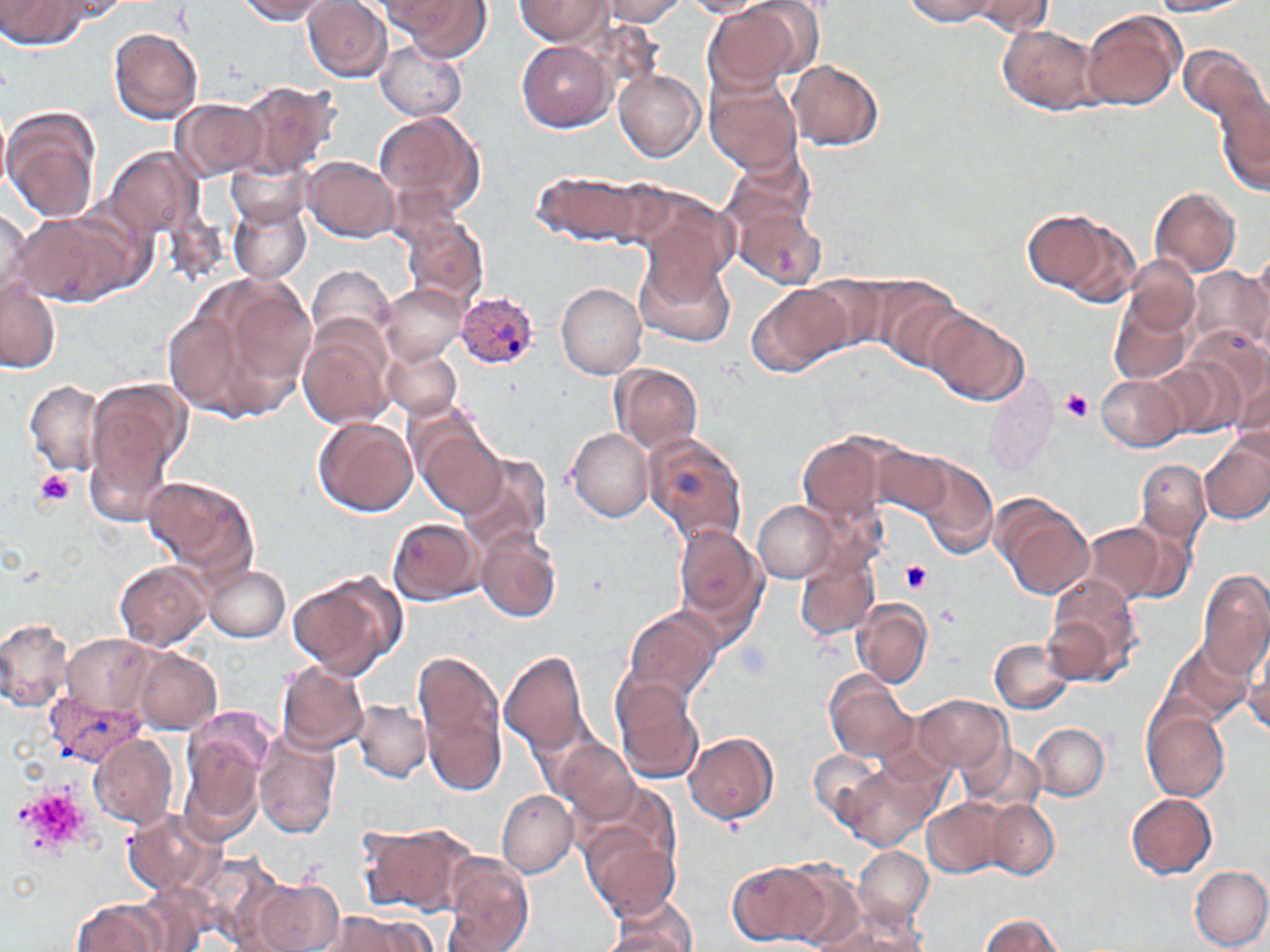

Approximate bounding boxes as [x1, y1, x2, y2] in pixels. Uninfected red blood cell locations: [2, 0, 91, 49], [235, 0, 340, 21], [515, 0, 612, 45], [1146, 0, 1253, 16], [304, 1, 395, 82], [390, 1, 493, 63], [597, 1, 688, 27], [681, 1, 768, 17], [904, 1, 1002, 25], [967, 1, 1049, 36], [704, 3, 815, 91], [1082, 11, 1185, 111], [998, 25, 1100, 115], [110, 27, 203, 123], [374, 39, 468, 123], [517, 41, 614, 131], [1180, 46, 1268, 163], [787, 59, 883, 150], [614, 69, 705, 162], [705, 74, 802, 175], [234, 80, 337, 178], [1214, 82, 1269, 201], [172, 98, 267, 181], [3, 106, 103, 225], [0, 110, 11, 193], [374, 110, 489, 225], [101, 145, 205, 246], [302, 156, 400, 242], [227, 160, 311, 229], [533, 168, 650, 246], [1152, 187, 1242, 275], [634, 188, 738, 296], [730, 200, 828, 291], [229, 203, 312, 283], [0, 207, 31, 307], [12, 209, 136, 308], [1021, 209, 1124, 296], [402, 215, 488, 306], [636, 249, 736, 349], [1245, 249, 1270, 340], [1125, 257, 1200, 336], [308, 266, 395, 349], [1189, 266, 1268, 354], [170, 274, 315, 424], [862, 275, 968, 369], [804, 278, 891, 358], [556, 281, 647, 379], [746, 281, 854, 378], [0, 282, 59, 374], [376, 283, 469, 365], [1110, 294, 1191, 385], [925, 308, 1030, 405], [298, 315, 395, 427], [1183, 327, 1268, 428], [382, 345, 464, 420], [1150, 358, 1245, 439], [612, 363, 703, 453], [1232, 372, 1270, 460], [1096, 375, 1183, 451], [82, 376, 187, 525], [23, 379, 107, 476], [984, 385, 1057, 478], [314, 416, 417, 517], [418, 422, 511, 517], [566, 426, 653, 522], [642, 432, 750, 549], [796, 433, 895, 526], [1200, 438, 1270, 524], [874, 444, 953, 518], [454, 449, 552, 557], [907, 454, 998, 558], [1135, 458, 1211, 549], [143, 475, 258, 578], [992, 494, 1095, 600], [754, 502, 838, 583], [764, 508, 872, 622], [389, 517, 484, 604], [1080, 520, 1171, 605], [673, 524, 768, 640], [476, 528, 562, 622], [796, 547, 882, 642], [114, 559, 210, 650], [202, 563, 291, 641], [1196, 569, 1270, 680], [287, 571, 403, 678], [1043, 576, 1144, 688], [853, 598, 932, 689], [620, 605, 723, 709], [0, 617, 76, 713], [1166, 633, 1259, 726], [63, 634, 153, 715], [1244, 634, 1270, 737], [990, 637, 1074, 713], [413, 648, 508, 794], [133, 649, 222, 733], [500, 651, 591, 757], [277, 662, 369, 754], [823, 671, 916, 761], [615, 676, 703, 783], [912, 695, 1010, 774], [354, 699, 430, 781], [1141, 705, 1230, 800], [180, 719, 274, 841], [1030, 723, 1109, 800], [685, 730, 780, 824], [91, 734, 177, 829], [253, 734, 340, 838], [554, 740, 637, 824], [965, 745, 1043, 814], [811, 747, 887, 826], [835, 758, 937, 849], [495, 788, 577, 877], [1127, 792, 1219, 878], [922, 796, 1010, 879], [986, 800, 1060, 879], [122, 808, 222, 896], [580, 818, 682, 923], [356, 820, 477, 916], [853, 846, 933, 926], [442, 856, 532, 950], [726, 858, 836, 946], [1190, 866, 1270, 950], [784, 867, 875, 950], [246, 875, 344, 952], [71, 897, 168, 952], [604, 900, 698, 951], [816, 909, 927, 952], [322, 912, 431, 951], [977, 913, 1066, 952], [595, 928, 694, 950]. Platelet locations: [1060, 391, 1092, 423], [33, 469, 75, 507], [900, 561, 932, 593], [940, 605, 960, 627], [735, 640, 772, 682], [14, 784, 87, 854]. Plasmodium vivax-infected red blood cell locations: [454, 290, 537, 368], [46, 689, 148, 769]. Slide-level diagnosis: Plasmodium vivax. Single field of view. May-Grünwald-Giemsa-stained preparation. Captured at 1000x magnification. Optical microscopy. Image is 1270×952 pixels. Thin blood smear.